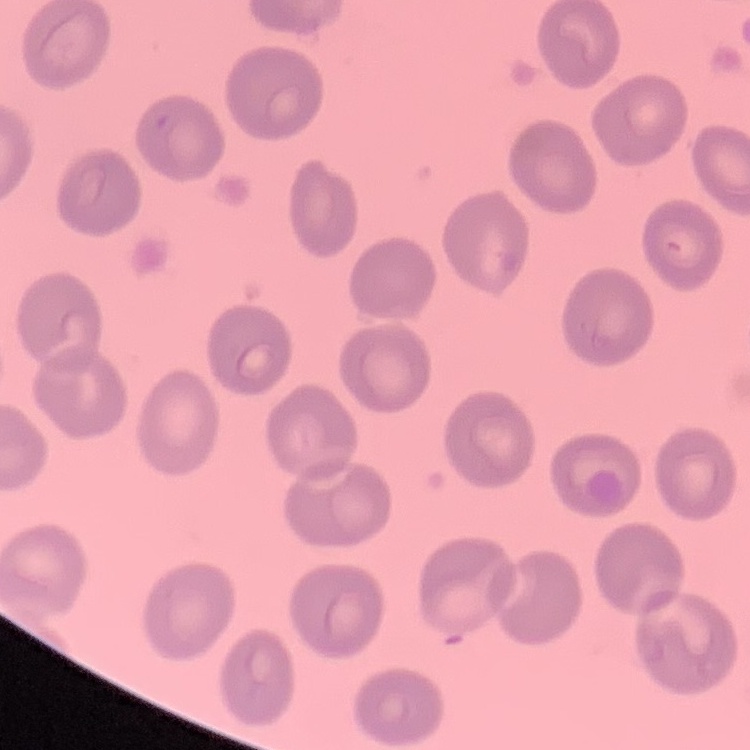
The red blood cells show no rouleaux formation. Thin blood film. Stained with either Field's or Giemsa. One tile cut from a larger photomicrograph.